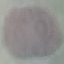
Summary:
  - Malaria status: uninfected
  - Capture: smartphone through the microscope eyepiece
  - Stain: Giemsa
  - Preparation: thin smear
  - Image type: automatically extracted cell patch, resized to 64 × 64 pixels